State which parasite is depicted.
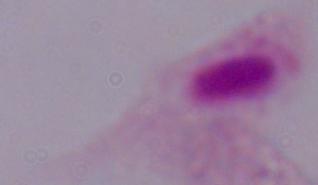

A trichomonad.

Summary:
  - Magnification: 1000x
  - Modality: photomicrograph